Report the malaria status of this cell.
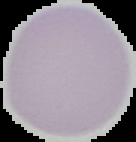

It is uninfected.

Summary:
  - Image type: segmented cell region on a black background
  - Image size: 136×142 pixels
  - Preparation: thin blood smear